Give the extent of all uninfected red blood cells.
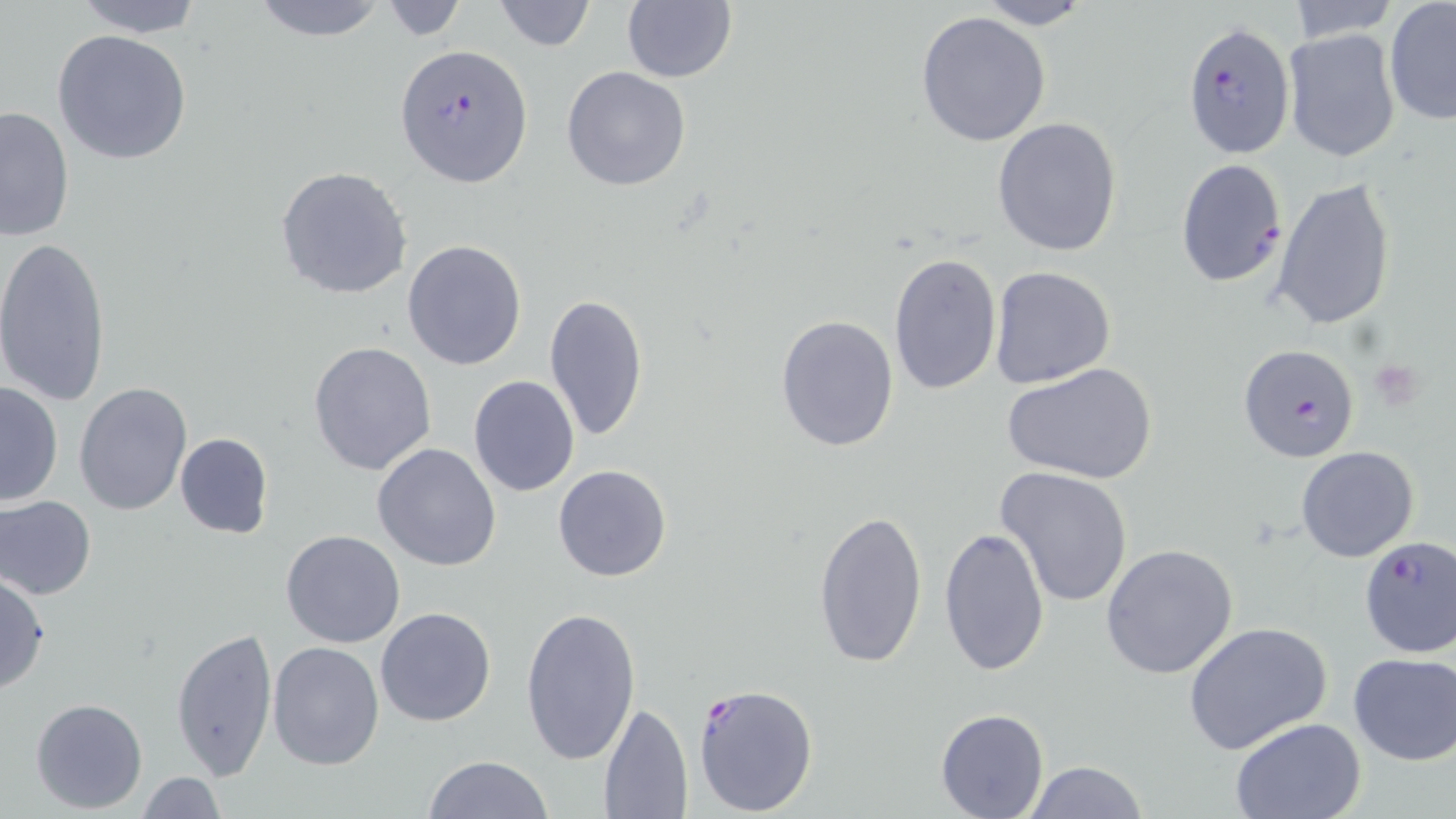
Approximate bounding boxes as [x1, y1, x2, y2] in pixels.
Uninfected red blood cells: [66, 0, 208, 37], [246, 0, 392, 43], [494, 0, 596, 51], [1285, 0, 1400, 44], [976, 1, 1092, 29], [377, 2, 469, 41], [621, 2, 737, 83], [1383, 3, 1456, 126], [914, 10, 1052, 148], [1284, 27, 1400, 162], [51, 30, 192, 164], [560, 66, 692, 192], [0, 105, 75, 243], [993, 117, 1123, 257], [275, 165, 412, 300], [1273, 176, 1396, 330], [0, 237, 112, 407], [403, 240, 527, 370], [887, 251, 1001, 399], [988, 266, 1116, 389], [544, 293, 649, 443], [774, 312, 899, 452], [308, 340, 438, 475], [1002, 361, 1158, 486], [468, 375, 579, 496], [1, 379, 64, 506], [75, 382, 193, 517], [175, 432, 273, 540], [373, 443, 502, 571], [1296, 446, 1420, 563], [554, 465, 672, 583], [994, 468, 1135, 611], [1, 494, 97, 599], [812, 507, 926, 668], [939, 525, 1050, 675], [280, 531, 404, 648], [1100, 544, 1240, 681], [0, 573, 49, 696], [518, 604, 643, 766], [374, 606, 498, 727], [1184, 621, 1334, 758], [171, 628, 279, 780], [266, 640, 384, 770], [1346, 653, 1455, 766], [31, 698, 148, 814], [598, 701, 692, 817], [935, 707, 1048, 817], [1232, 717, 1366, 818], [424, 755, 551, 819], [1023, 760, 1149, 818], [134, 772, 227, 819].

Summary:
  - Platelet locations: [1370, 361, 1427, 409]
  - Plasmodium falciparum-infected red blood cell locations: [1183, 20, 1295, 160], [395, 45, 532, 186], [1175, 159, 1287, 287], [1239, 342, 1361, 463], [1358, 535, 1456, 657], [690, 682, 819, 816]
  - Slide-level diagnosis: Plasmodium falciparum
  - Preparation: thin blood smear
  - Stain: May-Grünwald-Giemsa
  - Field of view: one of a larger specimen
  - Image size: 1456×819 pixels
  - Modality: light microscopy
  - Magnification: 1000x